Identify the blood parasite species.
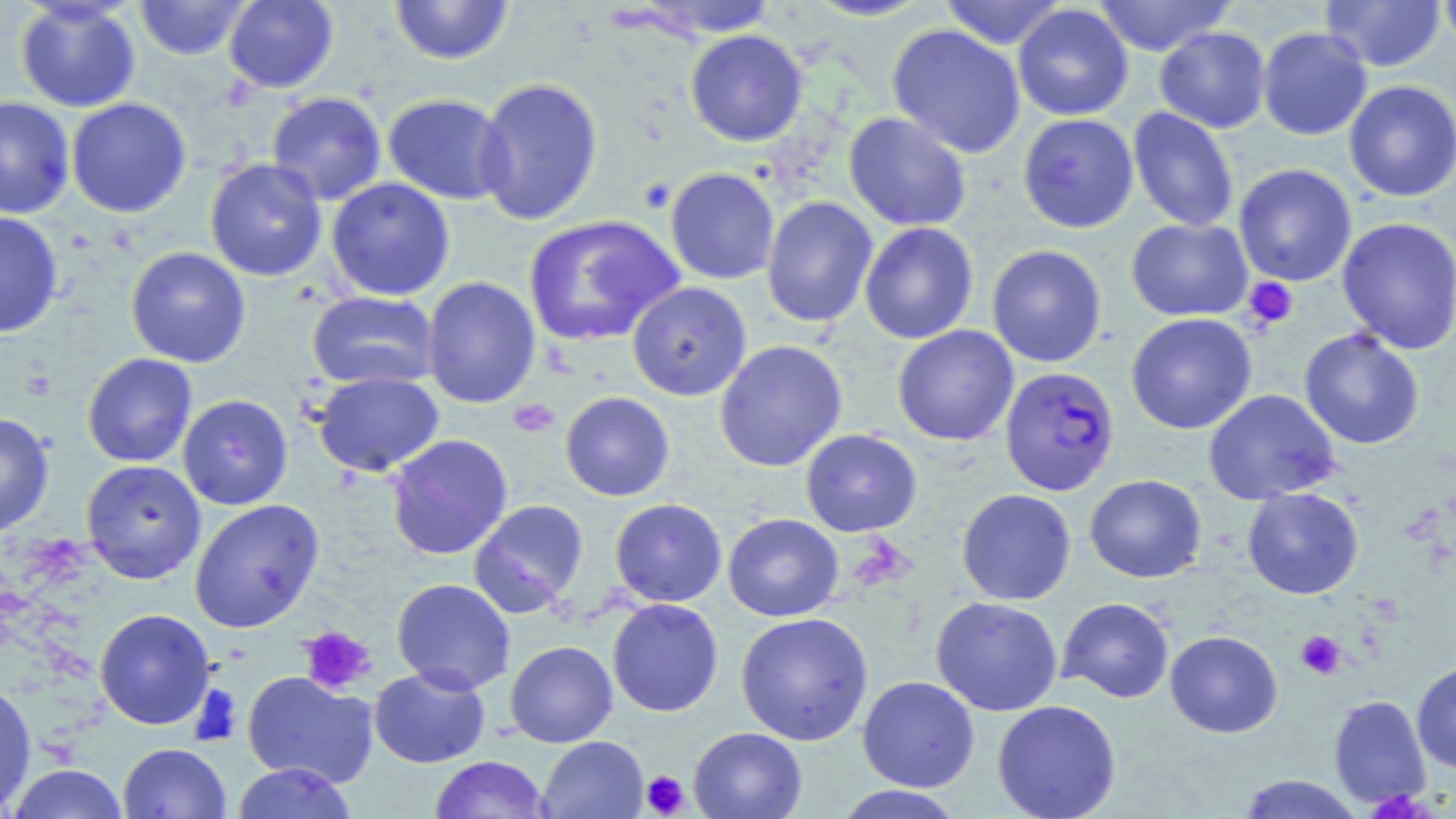

Plasmodium falciparum.

Approximate bounding boxes as (x1, y1, x2, y2) in pixels. Plasmodium falciparum-infected red blood cell locations: (999, 366, 1120, 496). Platelet locations: (1242, 276, 1298, 330), (508, 398, 560, 438), (299, 626, 376, 695), (1295, 630, 1346, 679), (190, 685, 244, 746), (641, 770, 689, 817). Uninfected red blood cell locations: (134, 0, 252, 60), (223, 0, 339, 93), (389, 0, 515, 66), (619, 0, 783, 40), (802, 0, 936, 22), (937, 0, 1071, 49), (1088, 0, 1238, 57), (1320, 0, 1447, 72), (1437, 0, 1456, 58), (14, 1, 141, 112), (1012, 4, 1134, 121), (886, 24, 1026, 159), (1154, 26, 1271, 133), (1257, 26, 1373, 141), (685, 29, 808, 147), (474, 77, 603, 226), (1343, 80, 1456, 202), (266, 91, 387, 206), (382, 93, 510, 205), (0, 96, 75, 219), (66, 97, 192, 218), (1128, 106, 1239, 233), (843, 112, 972, 232), (1017, 113, 1139, 233), (204, 158, 327, 282), (1233, 163, 1357, 287), (665, 167, 780, 285), (325, 177, 455, 301), (761, 196, 878, 329), (0, 211, 64, 338), (523, 214, 685, 348), (1125, 217, 1253, 322), (1336, 217, 1456, 354), (859, 222, 979, 345), (986, 244, 1107, 368), (125, 247, 251, 368), (422, 276, 541, 409), (626, 282, 751, 401), (306, 290, 441, 390), (1126, 313, 1257, 434), (892, 325, 1019, 446), (1298, 328, 1425, 450), (713, 339, 848, 472), (82, 353, 197, 468), (311, 371, 445, 476), (1203, 389, 1341, 506), (560, 391, 675, 501), (177, 394, 293, 510), (0, 412, 55, 537), (800, 429, 922, 537), (385, 434, 513, 560), (81, 459, 205, 584), (1084, 474, 1207, 583), (1242, 487, 1364, 600), (956, 488, 1076, 606), (189, 498, 324, 633), (609, 498, 727, 607), (468, 499, 589, 618), (723, 513, 844, 622), (391, 578, 516, 695), (930, 596, 1063, 716), (1057, 597, 1175, 703), (607, 598, 723, 717), (94, 608, 215, 730), (735, 612, 874, 745), (1165, 630, 1283, 738), (504, 641, 618, 748), (1411, 661, 1456, 774), (369, 665, 490, 768), (242, 671, 378, 788), (857, 675, 980, 792), (0, 682, 36, 815), (1329, 695, 1431, 809), (992, 700, 1121, 819), (689, 727, 807, 819), (537, 736, 649, 819), (118, 743, 231, 819), (429, 755, 551, 818), (231, 762, 357, 818), (4, 763, 130, 819), (1237, 773, 1365, 818), (832, 785, 967, 818). Thin blood film. 1000x magnification. Image is 1456×819 pixels. One field of a larger specimen. May-Grünwald-Giemsa-stained preparation. Optical microscopy.